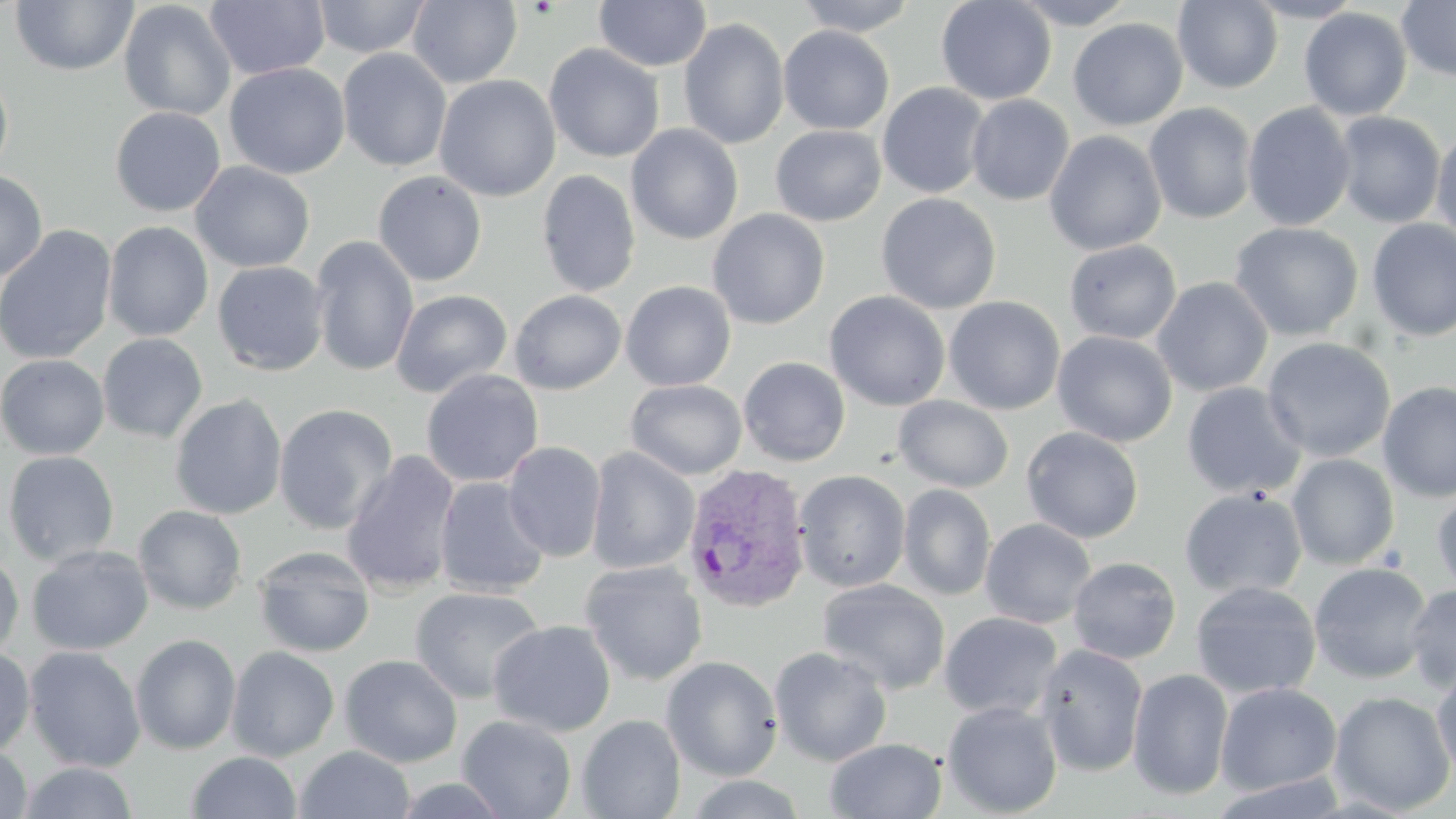 Approximate bounding boxes as named x1/y1/x2/y2 corners in pixels. Uninfected red blood cell locations: (x1=9, y1=0, x2=139, y2=76), (x1=205, y1=0, x2=330, y2=81), (x1=312, y1=0, x2=432, y2=59), (x1=594, y1=0, x2=712, y2=72), (x1=793, y1=0, x2=919, y2=36), (x1=935, y1=0, x2=1057, y2=105), (x1=1010, y1=0, x2=1139, y2=29), (x1=1244, y1=0, x2=1365, y2=23), (x1=1397, y1=0, x2=1456, y2=82), (x1=118, y1=1, x2=236, y2=121), (x1=407, y1=1, x2=523, y2=88), (x1=1173, y1=1, x2=1283, y2=93), (x1=1298, y1=7, x2=1412, y2=121), (x1=678, y1=18, x2=790, y2=150), (x1=1068, y1=18, x2=1188, y2=131), (x1=778, y1=25, x2=894, y2=135), (x1=543, y1=43, x2=665, y2=162), (x1=337, y1=48, x2=452, y2=172), (x1=224, y1=62, x2=351, y2=179), (x1=0, y1=67, x2=14, y2=181), (x1=434, y1=75, x2=561, y2=202), (x1=877, y1=82, x2=991, y2=199), (x1=966, y1=95, x2=1074, y2=206), (x1=1143, y1=103, x2=1258, y2=224), (x1=1242, y1=103, x2=1356, y2=231), (x1=110, y1=106, x2=226, y2=217), (x1=1333, y1=112, x2=1446, y2=228), (x1=626, y1=124, x2=744, y2=245), (x1=771, y1=125, x2=886, y2=227), (x1=1045, y1=130, x2=1166, y2=256), (x1=1431, y1=131, x2=1456, y2=248), (x1=191, y1=161, x2=315, y2=273), (x1=537, y1=169, x2=640, y2=297), (x1=0, y1=171, x2=47, y2=283), (x1=372, y1=171, x2=487, y2=286), (x1=876, y1=192, x2=1002, y2=315), (x1=707, y1=209, x2=830, y2=330), (x1=1366, y1=219, x2=1456, y2=342), (x1=103, y1=221, x2=213, y2=341), (x1=1229, y1=222, x2=1363, y2=341), (x1=0, y1=224, x2=118, y2=365), (x1=310, y1=235, x2=419, y2=377), (x1=1064, y1=240, x2=1182, y2=345), (x1=319, y1=254, x2=505, y2=391), (x1=212, y1=261, x2=329, y2=376), (x1=1152, y1=277, x2=1273, y2=397), (x1=621, y1=281, x2=736, y2=391), (x1=391, y1=289, x2=512, y2=398), (x1=509, y1=290, x2=627, y2=395), (x1=824, y1=291, x2=951, y2=411), (x1=944, y1=296, x2=1065, y2=415), (x1=1052, y1=331, x2=1177, y2=447), (x1=97, y1=333, x2=208, y2=443), (x1=1261, y1=337, x2=1396, y2=463), (x1=0, y1=354, x2=109, y2=460), (x1=738, y1=357, x2=851, y2=467), (x1=421, y1=369, x2=544, y2=488), (x1=625, y1=379, x2=747, y2=480), (x1=1377, y1=381, x2=1456, y2=503), (x1=1181, y1=382, x2=1307, y2=500), (x1=169, y1=394, x2=287, y2=520), (x1=893, y1=396, x2=1015, y2=493), (x1=273, y1=404, x2=398, y2=535), (x1=1021, y1=426, x2=1144, y2=543), (x1=502, y1=442, x2=607, y2=562), (x1=585, y1=447, x2=700, y2=575), (x1=341, y1=450, x2=461, y2=596), (x1=2, y1=451, x2=119, y2=565), (x1=1286, y1=453, x2=1400, y2=570), (x1=794, y1=470, x2=910, y2=593), (x1=435, y1=477, x2=550, y2=598), (x1=898, y1=484, x2=995, y2=601), (x1=1431, y1=485, x2=1456, y2=599), (x1=1179, y1=488, x2=1307, y2=600), (x1=133, y1=505, x2=247, y2=615), (x1=980, y1=518, x2=1096, y2=628), (x1=27, y1=545, x2=153, y2=655), (x1=253, y1=546, x2=375, y2=657), (x1=0, y1=553, x2=24, y2=663), (x1=1067, y1=556, x2=1181, y2=664), (x1=579, y1=560, x2=708, y2=686), (x1=1308, y1=562, x2=1433, y2=684), (x1=817, y1=578, x2=951, y2=695), (x1=1190, y1=581, x2=1321, y2=699), (x1=1405, y1=583, x2=1456, y2=692), (x1=410, y1=586, x2=545, y2=704), (x1=939, y1=611, x2=1063, y2=720), (x1=488, y1=620, x2=616, y2=737), (x1=131, y1=634, x2=241, y2=754), (x1=1034, y1=643, x2=1149, y2=777), (x1=24, y1=646, x2=146, y2=773), (x1=226, y1=646, x2=340, y2=761), (x1=769, y1=646, x2=893, y2=766), (x1=0, y1=647, x2=35, y2=756), (x1=339, y1=654, x2=463, y2=768), (x1=661, y1=655, x2=783, y2=781), (x1=1431, y1=664, x2=1456, y2=779), (x1=1127, y1=668, x2=1233, y2=801), (x1=1215, y1=683, x2=1342, y2=796), (x1=1329, y1=691, x2=1454, y2=815), (x1=942, y1=700, x2=1063, y2=817), (x1=457, y1=714, x2=576, y2=819), (x1=577, y1=714, x2=686, y2=819), (x1=825, y1=737, x2=947, y2=819), (x1=0, y1=743, x2=34, y2=818), (x1=295, y1=745, x2=415, y2=819), (x1=186, y1=751, x2=302, y2=818), (x1=18, y1=762, x2=140, y2=819), (x1=679, y1=773, x2=812, y2=818), (x1=386, y1=775, x2=515, y2=818). Plasmodium vivax-infected red blood cell locations: (x1=681, y1=464, x2=812, y2=614). Slide-level diagnosis: Plasmodium vivax. Thin blood smear. Captured at 1000x magnification. May-Grünwald-Giemsa stain. Single field of view. Image is 1456×819 pixels. Optical microscopy.